Assess the morphology of the red blood cells.
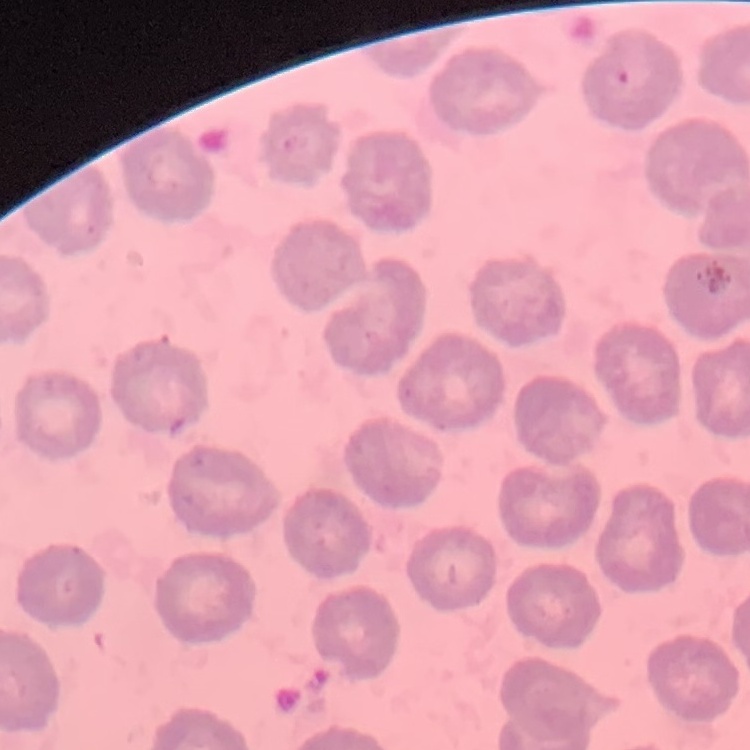

They show no rouleaux formation.

Thin blood film. Stained with either Field's or Giemsa. One tile cut from a larger photomicrograph.